Identify the parasite.
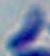
Toxoplasma gondii.

Summary:
  - Modality: photomicrograph
  - Magnification: 1000x